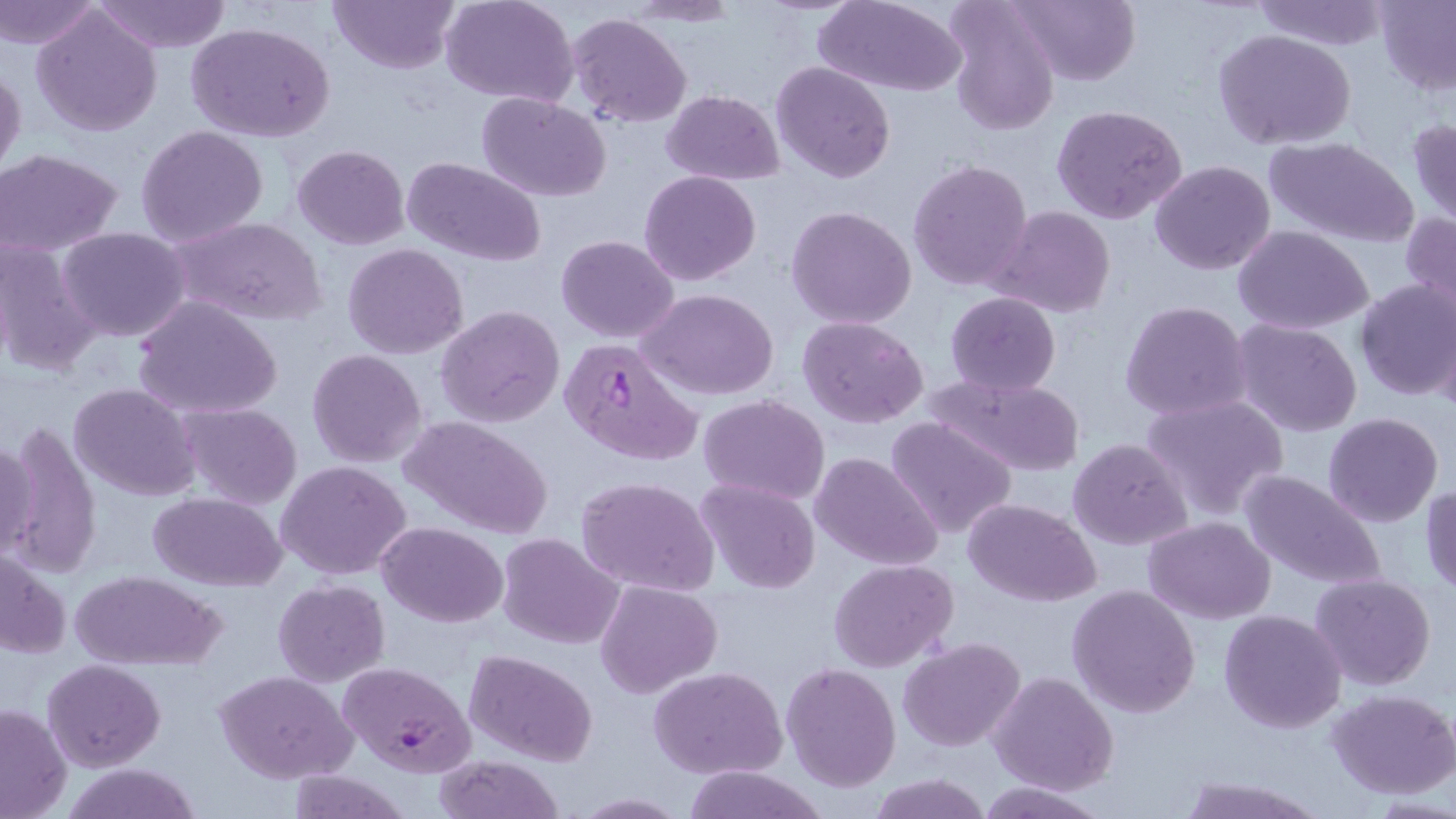

slide_level_diagnosis: Plasmodium falciparum
image_size: 1456×819 pixels
magnification: 1000x
preparation: thin blood film
field_of_view: one of a larger specimen
uninfected_red_blood_cell_locations: 'approximate bounding boxes as (x1, y1, x2, y2) in pixels: (0, 0, 103, 49), (91, 0, 233, 53), (329, 0, 459, 74), (441, 0, 579, 106), (946, 0, 1061, 137), (1010, 0, 1140, 87), (1251, 0, 1391, 50), (1373, 0, 1456, 95), (815, 2, 966, 95), (31, 4, 163, 136), (566, 13, 691, 128), (187, 21, 337, 145), (1214, 29, 1356, 151), (770, 61, 895, 184), (0, 65, 26, 182), (661, 90, 786, 184), (476, 92, 612, 202), (1051, 104, 1187, 224), (1407, 118, 1456, 231), (136, 125, 268, 246), (1261, 136, 1417, 247), (292, 144, 409, 249), (0, 149, 123, 255), (401, 155, 547, 266), (907, 158, 1034, 292), (1149, 160, 1277, 275), (640, 171, 761, 286), (786, 205, 918, 330), (987, 205, 1115, 319), (1400, 212, 1456, 322), (170, 216, 326, 327), (1232, 225, 1375, 334), (58, 227, 191, 342), (556, 234, 678, 343), (0, 235, 100, 377), (343, 244, 468, 359), (1354, 279, 1456, 402), (641, 288, 780, 400), (945, 291, 1062, 395), (132, 297, 282, 420), (1119, 300, 1253, 422), (436, 305, 566, 427), (798, 315, 928, 427), (1233, 319, 1362, 438), (306, 348, 427, 467), (932, 373, 1086, 474), (69, 382, 201, 501), (1140, 393, 1289, 521), (700, 394, 829, 505), (177, 402, 303, 510), (1322, 412, 1444, 528), (401, 415, 554, 539), (885, 416, 1018, 539), (5, 424, 102, 578), (1, 431, 40, 563), (1068, 438, 1193, 550), (812, 451, 943, 571), (276, 460, 411, 580), (1239, 468, 1386, 591), (576, 476, 719, 597), (695, 479, 820, 593), (1420, 484, 1456, 597), (148, 492, 288, 590), (963, 498, 1101, 604), (1143, 516, 1277, 622), (378, 521, 507, 627), (497, 532, 623, 649), (0, 547, 71, 661), (830, 559, 958, 673), (69, 568, 228, 671), (1309, 573, 1437, 693), (272, 579, 390, 687), (596, 579, 722, 700), (1068, 584, 1202, 719), (1218, 608, 1347, 733), (899, 637, 1024, 752), (465, 649, 598, 766), (42, 658, 166, 771), (780, 662, 902, 792), (648, 665, 788, 780), (215, 670, 358, 783), (988, 670, 1117, 796), (1327, 688, 1456, 799), (0, 703, 72, 818), (434, 755, 567, 819), (62, 763, 200, 819), (678, 766, 828, 819), (286, 771, 412, 817), (866, 773, 995, 819), (1174, 775, 1328, 818), (975, 780, 1108, 818), (572, 793, 690, 817)'
modality: optical microscopy
plasmodium_falciparum_infected_red_blood_cell_locations: 'approximate bounding boxes as (x1, y1, x2, y2) in pixels: (557, 336, 702, 467), (338, 661, 477, 780)'
stain: May-Grünwald-Giemsa